Assess the morphology of the red blood cells.
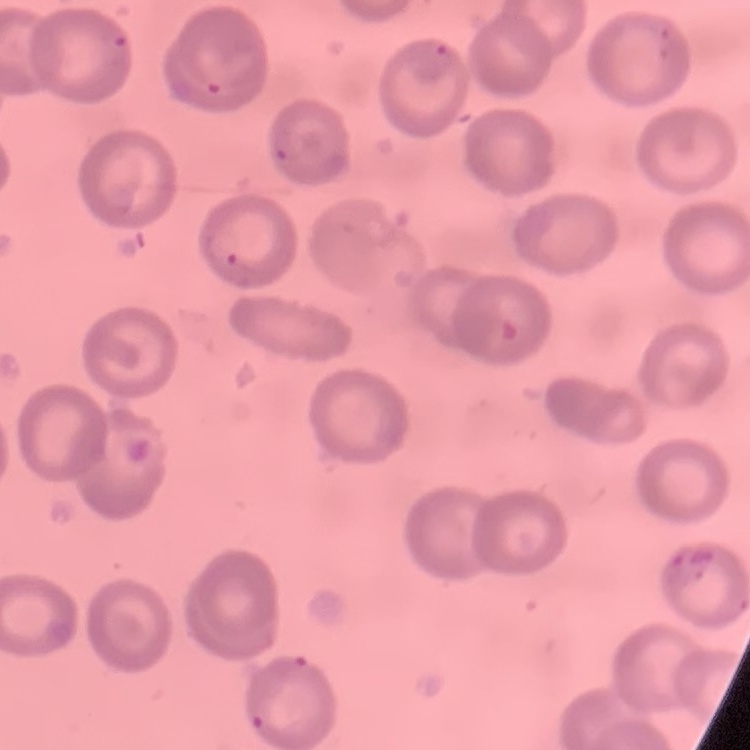

They show no rouleaux formation.

Summary:
  - Image type: one tile cut from a larger photomicrograph
  - Preparation: thin blood smear
  - Stain: Field's or Giemsa